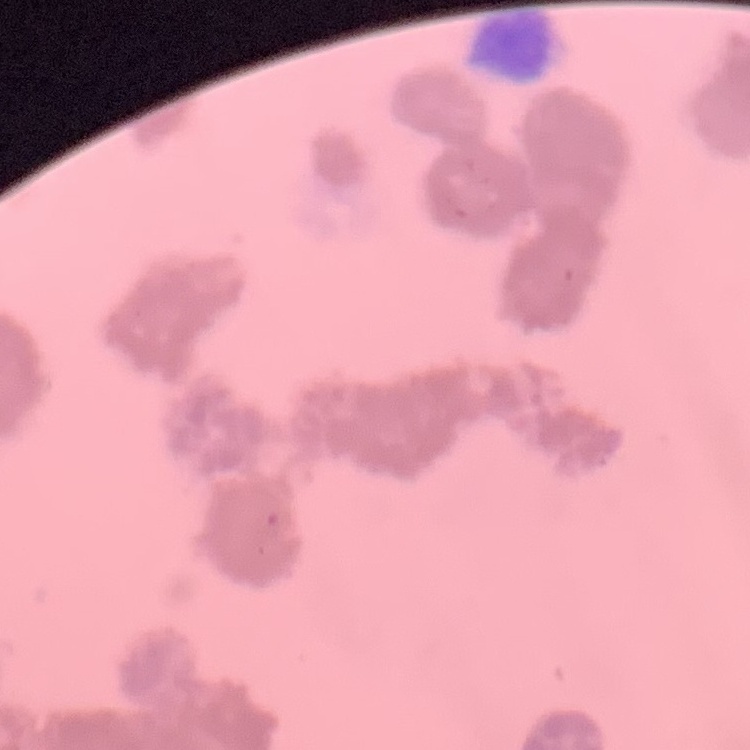

The red blood cells show rouleaux formation. One tile cut from a larger photomicrograph. Field's or Giemsa stain. Thin peripheral smear.